Locate platelets.
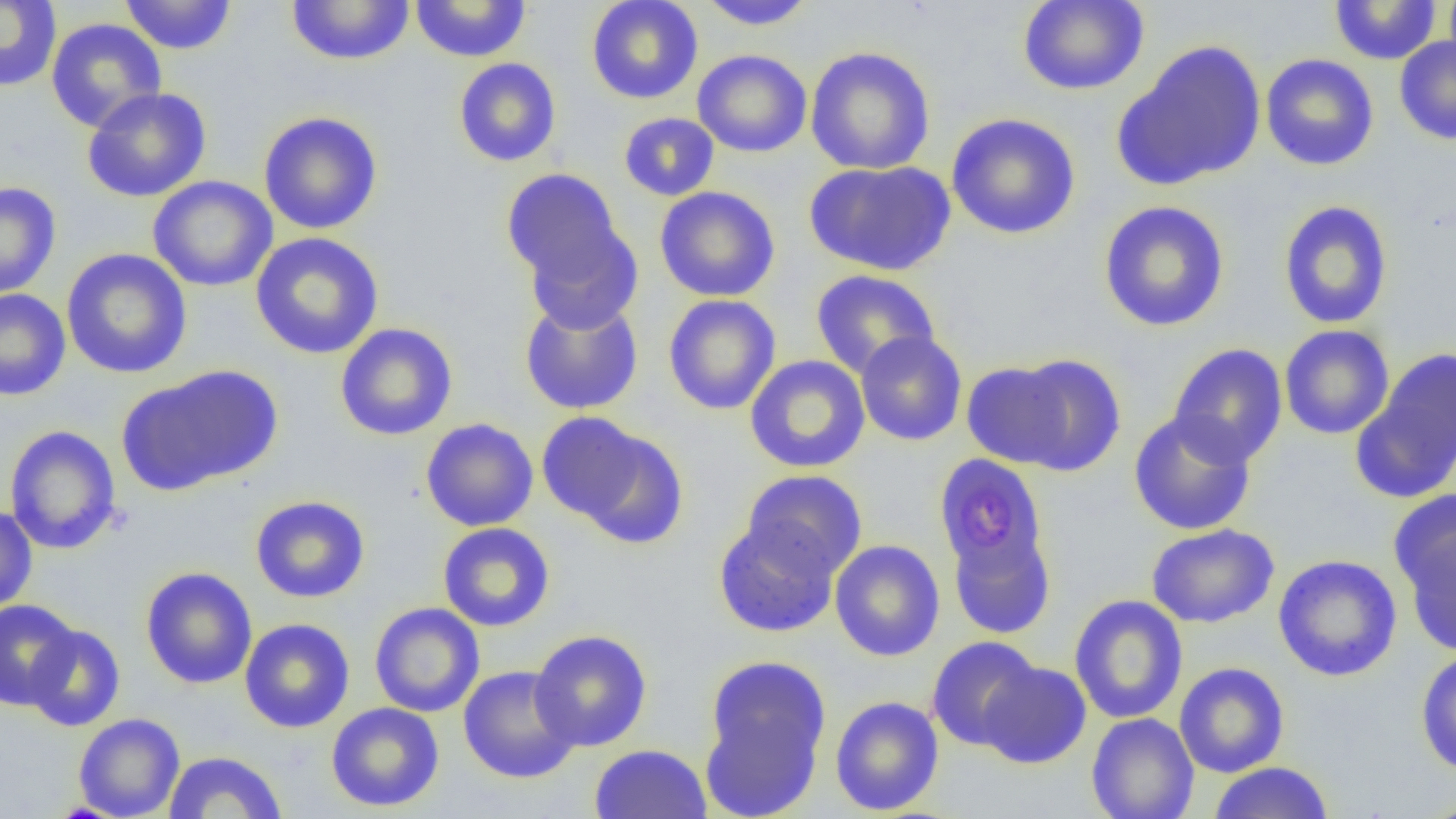

Approximate bounding boxes as [x1, y1, x2, y2] in pixels.
Platelets: [959, 490, 1018, 550].

slide-level diagnosis = negative for blood parasites
magnification = 1000x
modality = light microscopy
field of view = single
preparation = thin blood smear
uninfected red blood cell locations = approximate bounding boxes as [x1, y1, x2, y2] in pixels: [120, 0, 237, 55], [285, 0, 416, 66], [586, 0, 703, 104], [1017, 0, 1149, 96], [1444, 0, 1456, 78], [0, 1, 62, 92], [409, 1, 532, 62], [697, 1, 816, 30], [1329, 1, 1443, 65], [46, 17, 167, 133], [1394, 36, 1456, 145], [1114, 40, 1267, 191], [805, 47, 936, 175], [692, 49, 812, 157], [1260, 53, 1379, 171], [453, 57, 562, 167], [82, 87, 212, 203], [258, 111, 383, 235], [618, 112, 719, 201], [946, 112, 1081, 239], [804, 159, 955, 276], [501, 168, 624, 288], [148, 175, 278, 292], [0, 181, 61, 298], [654, 187, 781, 302], [1098, 200, 1230, 332], [1277, 200, 1394, 329], [524, 223, 643, 333], [250, 232, 384, 360], [61, 248, 192, 379], [810, 269, 940, 378], [0, 289, 71, 401], [662, 294, 781, 415], [519, 297, 644, 415], [335, 323, 458, 441], [1279, 324, 1395, 440], [855, 331, 967, 446], [1168, 343, 1288, 467], [1354, 347, 1456, 501], [1007, 353, 1128, 476], [745, 355, 871, 473], [961, 360, 1074, 468], [122, 366, 281, 493], [536, 411, 654, 527], [1128, 411, 1256, 535], [420, 418, 539, 531], [4, 425, 121, 555], [570, 426, 689, 549], [934, 454, 1049, 575], [741, 469, 868, 580], [250, 495, 370, 603], [0, 505, 38, 615], [1397, 516, 1456, 656], [713, 519, 841, 638], [437, 522, 555, 632], [948, 524, 1057, 639], [1145, 524, 1279, 628], [829, 539, 945, 662], [1273, 554, 1403, 681], [140, 566, 258, 689], [1068, 594, 1188, 724], [0, 598, 80, 709], [369, 602, 485, 718], [239, 618, 355, 733], [24, 625, 125, 731], [529, 629, 652, 752], [926, 636, 1044, 751], [1415, 650, 1456, 776], [701, 654, 831, 816], [977, 660, 1092, 769], [1174, 662, 1290, 777], [458, 665, 581, 784], [829, 695, 944, 816], [326, 702, 444, 812], [73, 713, 185, 819], [1086, 713, 1199, 819], [589, 743, 712, 819], [163, 751, 287, 818], [1207, 762, 1334, 819], [1417, 794, 1456, 818]
image size = 1456×819 pixels